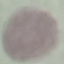

Result: no malaria parasites detected. Thin smear of blood. Photographed with a smartphone camera at the microscope eyepiece. Giemsa-stained preparation. Automatically extracted cell patch, resized to 64 × 64 pixels.